Identify the parasite.
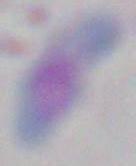

Toxoplasma gondii.

modality = photomicrograph
magnification = 1000x